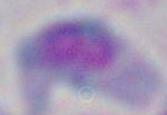
Micrograph. 1000x magnification. Toxoplasma gondii is shown.